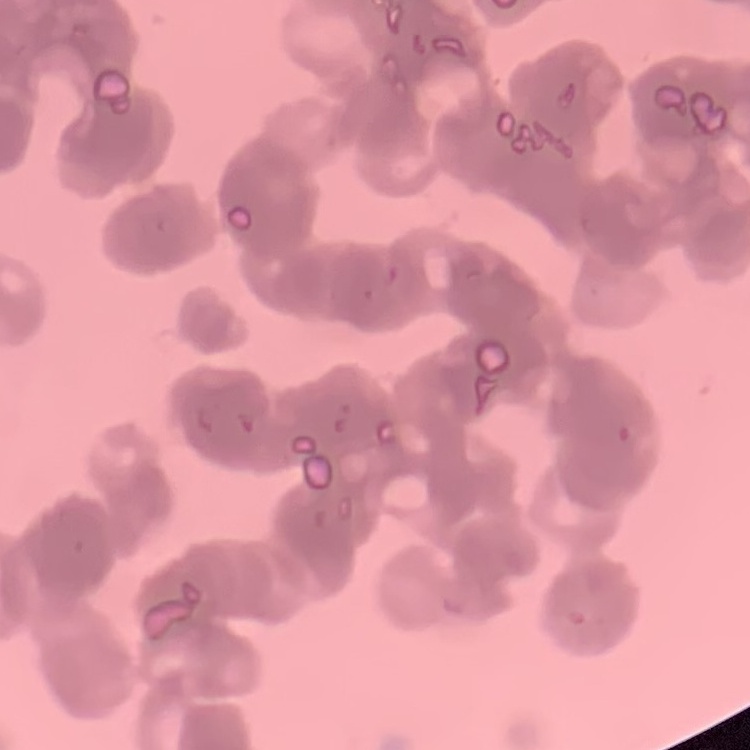
red blood cell morphology = rouleaux formation
preparation = thin blood film
image type = square crop of a larger photomicrograph
stain = Field's or Giemsa